Identify the parasite.
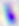
Toxoplasma gondii.

magnification: 400x
modality: photomicrograph